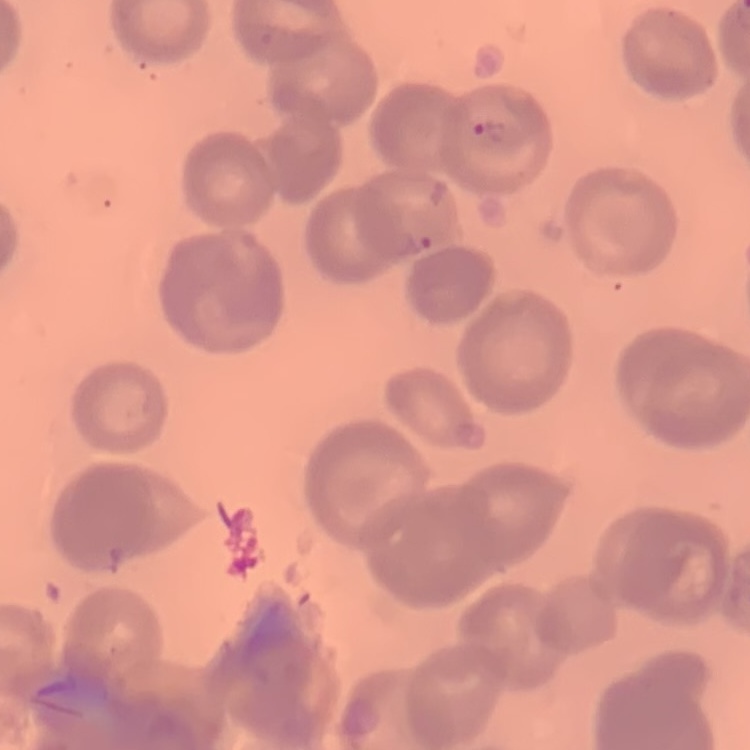 The erythrocytes show no rouleaux formation. Thin blood film. Stained with either Field's or Giemsa. Square crop of a larger photomicrograph.